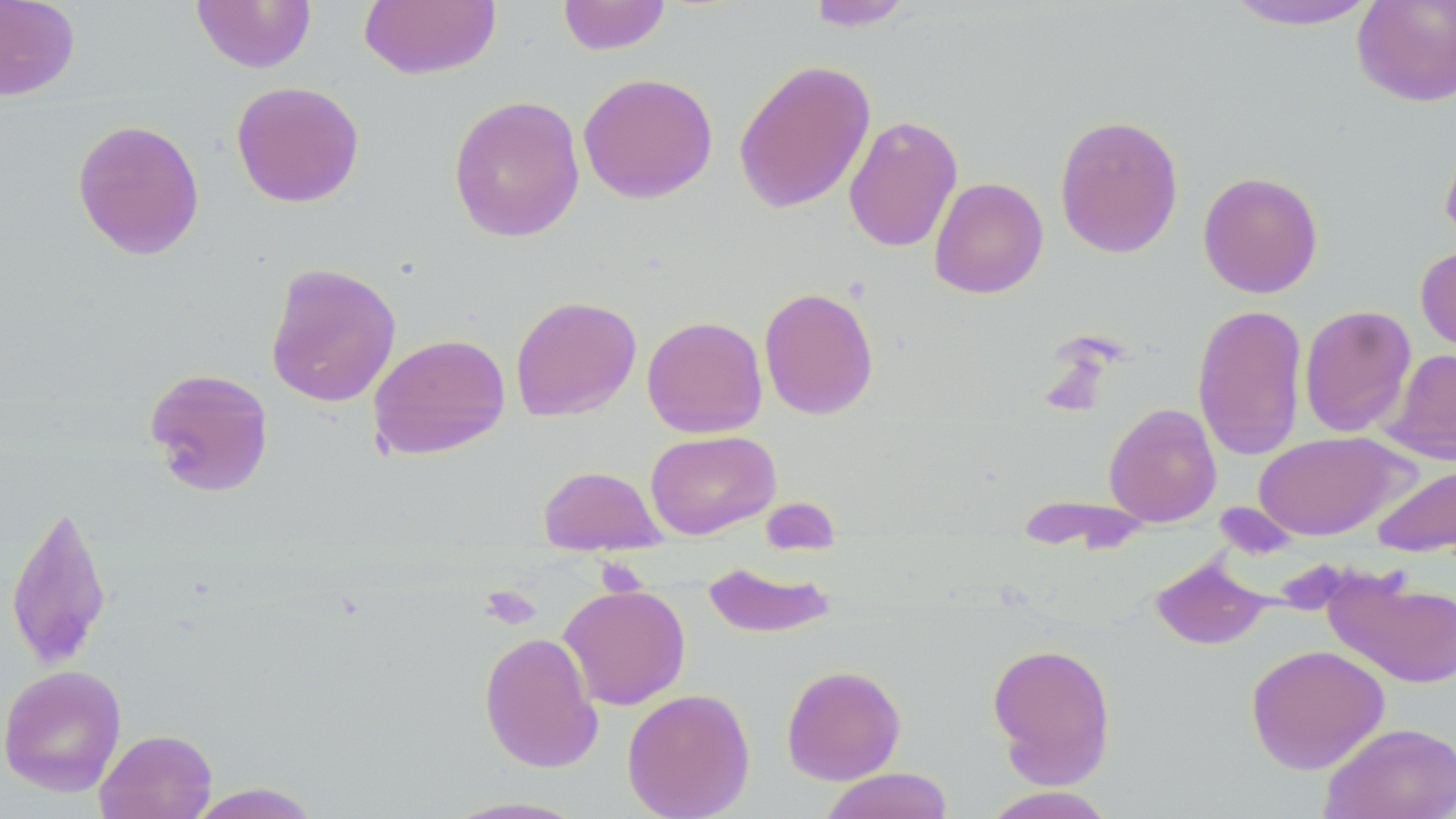
Approximate bounding boxes as (x1, y1, x2, y2) in pixels. Uninfected red blood cell locations: (0, 0, 80, 101), (359, 0, 501, 80), (557, 0, 672, 55), (1220, 0, 1384, 31), (1352, 0, 1456, 107), (191, 1, 316, 73), (804, 1, 915, 31), (733, 59, 876, 214), (578, 71, 718, 204), (230, 81, 365, 208), (448, 94, 585, 243), (1054, 113, 1184, 259), (843, 115, 963, 253), (71, 118, 205, 260), (1439, 128, 1456, 252), (1198, 171, 1324, 298), (929, 177, 1049, 299), (1415, 243, 1456, 362), (264, 262, 402, 408), (759, 286, 879, 420), (510, 295, 642, 421), (1192, 304, 1308, 461), (1299, 304, 1417, 438), (642, 315, 768, 437), (368, 333, 511, 461), (1383, 347, 1455, 466), (144, 367, 275, 497), (1104, 402, 1222, 527), (644, 430, 780, 539), (1254, 431, 1408, 541), (1372, 462, 1456, 557), (538, 465, 665, 554), (1015, 493, 1153, 556), (5, 500, 114, 672), (1150, 555, 1273, 651), (702, 561, 837, 639), (1324, 570, 1456, 689), (559, 583, 691, 710), (478, 631, 603, 774), (986, 642, 1117, 787), (1245, 643, 1390, 774), (0, 664, 127, 797), (781, 664, 906, 785), (621, 687, 756, 819), (1320, 721, 1456, 819), (95, 729, 217, 819), (818, 768, 955, 819), (185, 782, 324, 818), (977, 786, 1120, 818), (440, 795, 593, 818). Platelet locations: (480, 584, 541, 630). Slide-level diagnosis: negative for blood parasites. May-Grünwald-Giemsa stain. Light microscopy. Image is 1456×819 pixels. Thin blood smear. 1000x magnification. Single field of view.